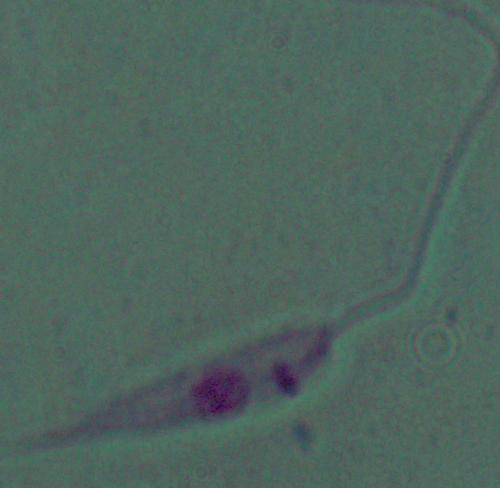

identification = Leishmania
modality = micrograph
magnification = 1000x